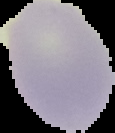

Summary:
  - Preparation: thin blood smear
  - Image size: 115×133 pixels
  - Image type: segmented cell region with the area outside set to black
  - Malaria status: uninfected